Report the malaria status of this cell.
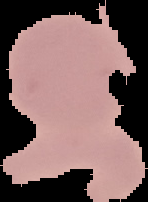
Uninfected.

Summary:
  - Image size: 148×202 pixels
  - Image type: segmented cell region with the area outside set to black
  - Preparation: thin blood smear